Report the malaria status of this cell.
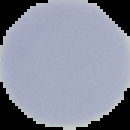

Uninfected.

Summary:
  - Preparation: thin blood smear
  - Image size: 130×130 pixels
  - Image type: segmented cell region on a black background